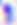

identification = Toxoplasma gondii
magnification = 400x
modality = micrograph